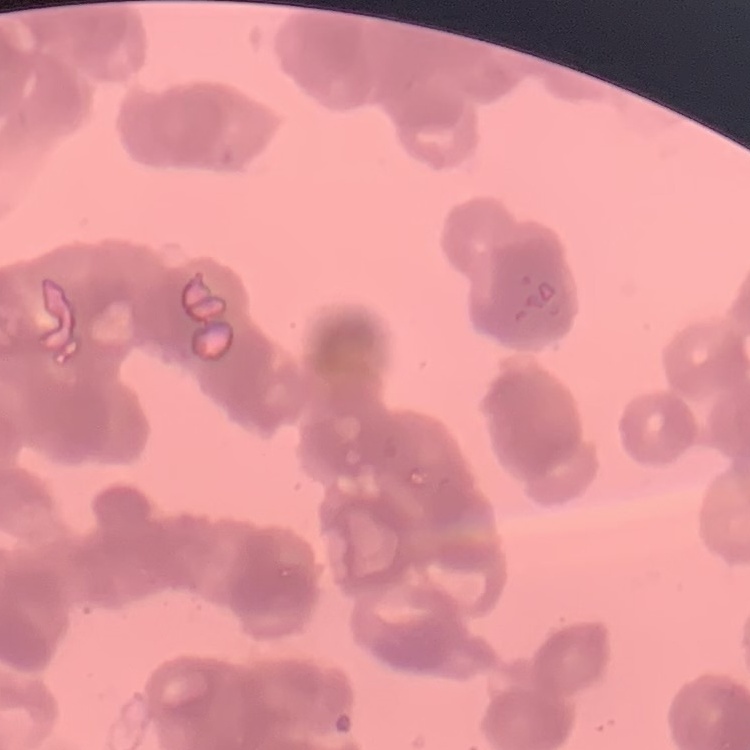
{
  "red_blood_cell_morphology": "rouleaux formation",
  "preparation": "thin blood smear",
  "image_type": "square crop of a larger photomicrograph",
  "stain": "Field's or Giemsa"
}